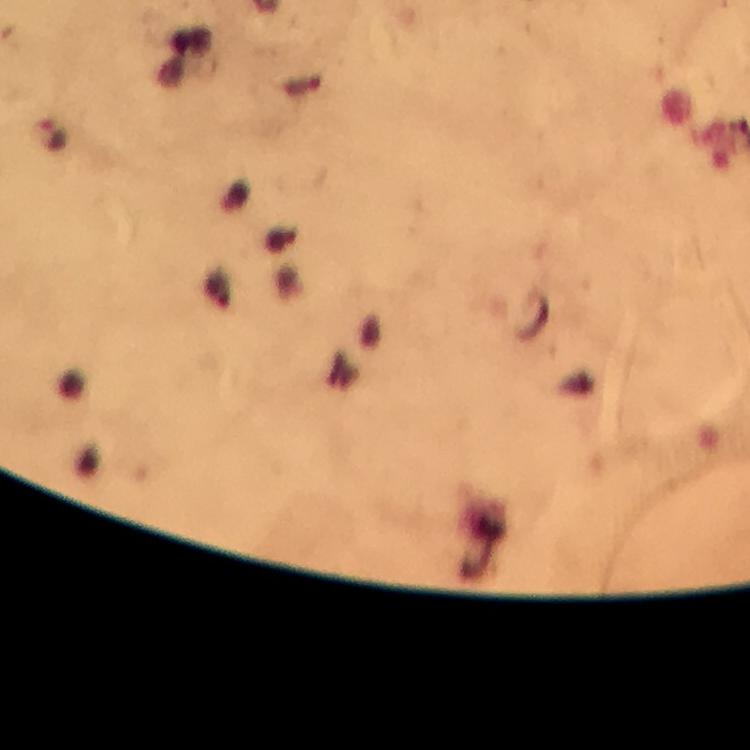

Approximate centers as [x, y] in pixels.
Summary:
  - Plasmodium parasite locations: [53, 137]
  - Preparation: thick smear
  - Magnification: 100x
  - Image size: 750×750 pixels
  - Cropped from: a single field of view
  - Stain: Giemsa
  - Context: from a malaria diagnostic workup
  - Capture: smartphone camera through the microscope
  - Immersion oil: used